Outline each blood parasite and name the species.
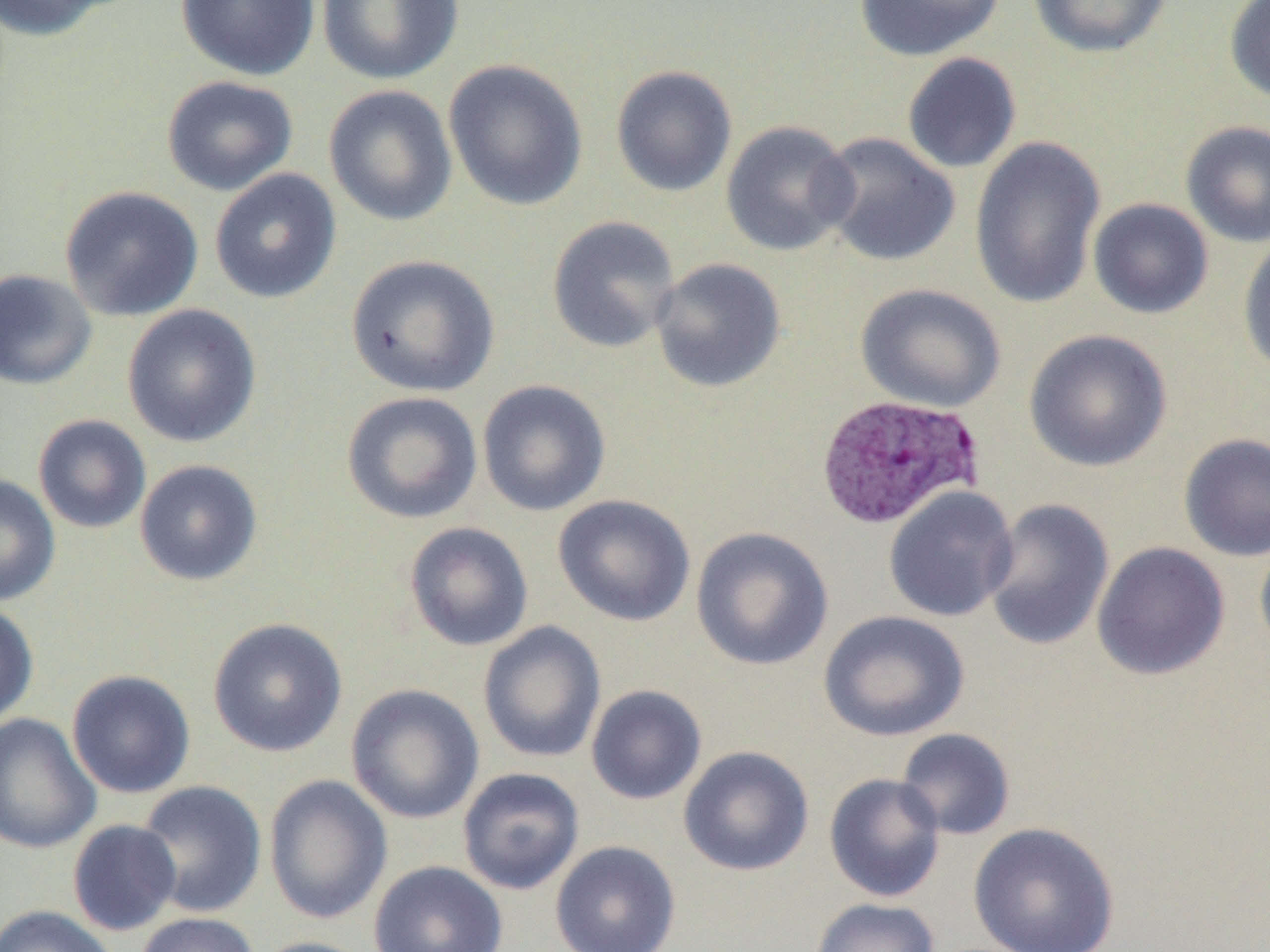

Approximate bounding boxes as (x1, y1, x2, y2) in pixels.
Plasmodium vivax-infected red blood cells: (815, 393, 986, 530).
No Plasmodium falciparum, Plasmodium ovale, Plasmodium malariae, Babesia divergens, or Trypanosoma brucei observed.

slide_level_diagnosis: Plasmodium vivax
image_size: 1270×952 pixels
preparation: thin blood smear
magnification: 1000x
field_of_view: one of a larger specimen
modality: optical microscopy
uninfected_red_blood_cell_locations: 'approximate bounding boxes as (x1, y1, x2, y2) in pixels: (0, 0, 112, 41), (175, 0, 320, 81), (317, 0, 463, 85), (853, 0, 1005, 61), (1027, 0, 1173, 58), (1224, 1, 1270, 103), (901, 52, 1022, 173), (443, 58, 588, 211), (611, 64, 737, 197), (161, 75, 298, 196), (323, 85, 459, 226), (1180, 119, 1270, 248), (720, 120, 858, 257), (817, 132, 962, 267), (969, 136, 1106, 310), (209, 168, 342, 304), (59, 186, 204, 322), (1088, 198, 1214, 319), (546, 215, 681, 353), (1238, 234, 1270, 377), (345, 254, 500, 398), (651, 257, 787, 393), (0, 268, 97, 390), (855, 283, 1007, 413), (122, 304, 262, 448), (1024, 328, 1173, 472), (476, 379, 611, 517), (341, 391, 483, 525), (32, 414, 152, 534), (1178, 432, 1270, 562), (134, 459, 263, 586), (0, 474, 61, 606), (883, 485, 1019, 622), (553, 494, 696, 627), (983, 498, 1115, 651), (403, 521, 534, 652), (690, 526, 834, 671), (1254, 532, 1270, 662), (1091, 541, 1231, 681), (0, 602, 39, 728), (819, 610, 969, 742), (207, 617, 348, 757), (478, 621, 607, 764), (66, 669, 196, 799), (346, 683, 485, 824), (585, 684, 707, 805), (0, 711, 101, 854), (895, 727, 1016, 840), (678, 745, 815, 877), (457, 767, 585, 895), (824, 773, 946, 903), (263, 774, 393, 925), (135, 780, 267, 918), (67, 819, 182, 936), (968, 821, 1120, 952), (549, 840, 681, 952), (368, 860, 508, 952), (809, 897, 941, 952), (0, 905, 119, 952), (134, 912, 260, 952), (251, 936, 378, 952)'